Assess the morphology of the erythrocytes.
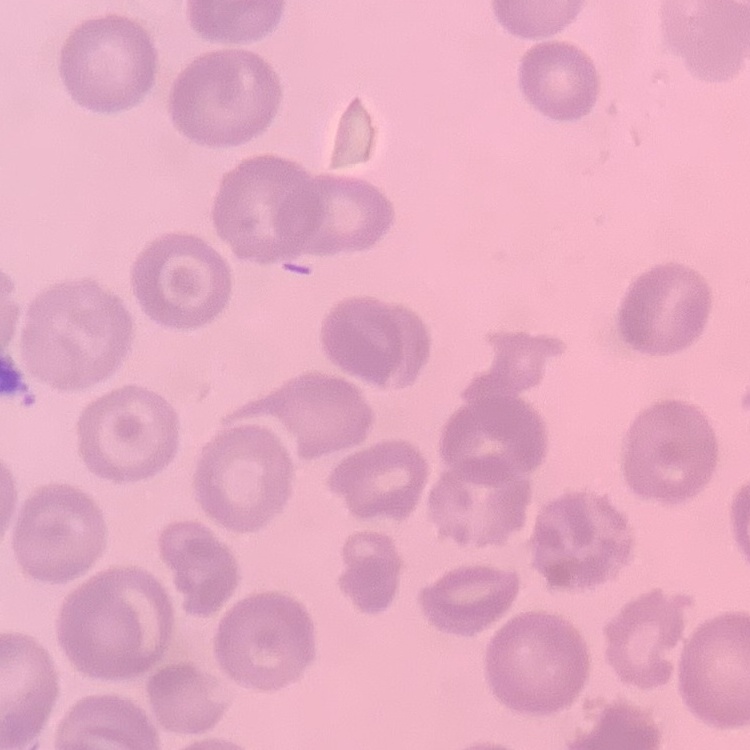

No rouleaux formation.

Summary:
  - Image type: one tile cut from a larger photomicrograph
  - Stain: Field's or Giemsa
  - Preparation: thin peripheral smear